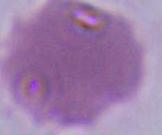 Micrograph. A red blood cell is seen. 1000x magnification.